Name the parasite shown.
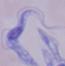

A trypanosome.

Photomicrograph. 1000x magnification.